Name the parasite shown.
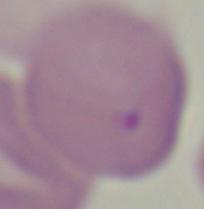

This is Babesia.

1000x magnification. Micrograph.